Report the malaria status of this cell.
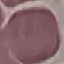

It is uninfected.

Giemsa-stained preparation. Acquired by smartphone through the microscope eyepiece. Automatically extracted cell patch, resized to 64 × 64 pixels. Thin smear of blood.